Classify this cell by malaria status.
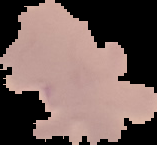
It is parasitized.

Summary:
  - Image size: 157×145 pixels
  - Image type: segmented cell region on a black background
  - Preparation: thin blood film